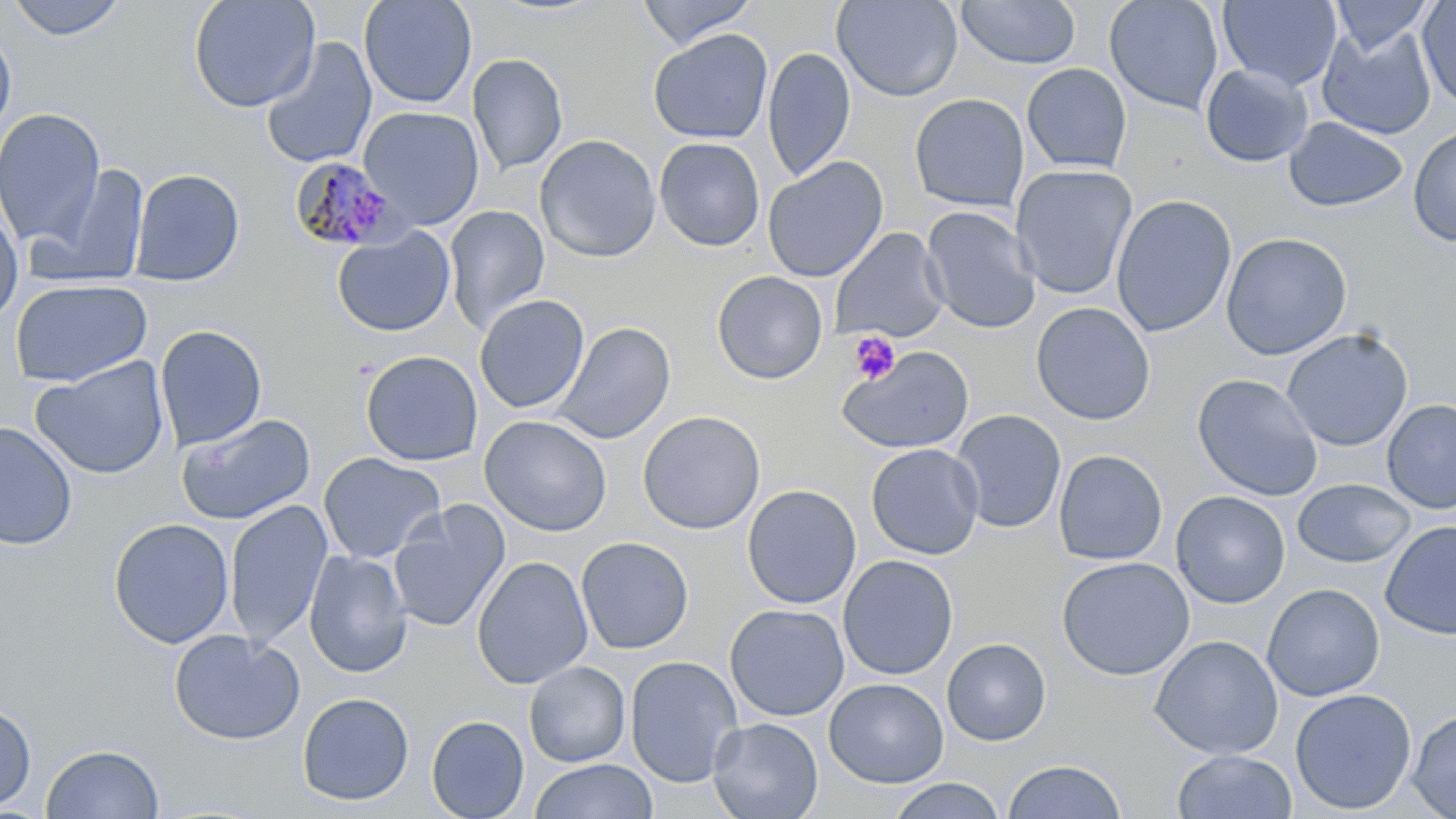
Approximate bounding boxes as (x1,y1)-(x2,y2) corner pairs in pixels. Platelet locations: (848,332)-(900,385). Plasmodium malariae-infected red blood cell locations: (288,156)-(405,254). Uninfected red blood cell locations: (6,0)-(129,42), (188,0)-(320,113), (359,0)-(477,109), (636,0)-(759,49), (832,0)-(963,102), (956,0)-(1081,69), (1104,0)-(1224,116), (1218,0)-(1342,91), (1330,0)-(1435,58), (1416,1)-(1456,109), (1317,25)-(1437,140), (0,26)-(16,140), (648,28)-(773,144), (259,37)-(378,170), (762,46)-(856,182), (467,53)-(568,175), (1021,62)-(1132,175), (1200,63)-(1314,168), (909,93)-(1029,212), (358,106)-(484,229), (0,107)-(105,248), (1283,116)-(1408,212), (1407,123)-(1456,247), (535,134)-(661,263), (654,137)-(765,251), (762,156)-(889,282), (29,164)-(151,289), (1011,164)-(1138,300), (129,168)-(245,286), (1111,194)-(1237,338), (0,203)-(24,325), (443,204)-(550,335), (920,206)-(1042,334), (332,227)-(455,337), (830,228)-(950,343), (1220,232)-(1353,360), (712,271)-(828,384), (10,278)-(153,387), (474,294)-(590,414), (1031,301)-(1156,425), (552,322)-(675,444), (155,325)-(268,450), (1281,328)-(1413,451), (837,345)-(974,454), (360,350)-(483,466), (31,357)-(170,480), (1191,373)-(1323,501), (1381,399)-(1456,514), (951,409)-(1067,534), (637,410)-(765,535), (175,413)-(316,526), (479,415)-(612,537), (191,416)-(326,632), (0,422)-(78,551), (866,443)-(984,560), (1053,449)-(1168,565), (318,452)-(445,564), (1292,478)-(1416,568), (741,484)-(861,609), (1171,491)-(1290,608), (224,500)-(333,649), (388,501)-(510,633), (108,517)-(234,649), (1380,520)-(1456,640), (575,536)-(694,654), (303,550)-(413,677), (838,554)-(958,681), (472,555)-(593,690), (1056,556)-(1195,681), (1262,583)-(1385,701), (724,603)-(850,722), (169,629)-(304,745), (1149,634)-(1284,759), (942,638)-(1051,746), (624,655)-(744,787), (524,661)-(630,767), (824,678)-(949,788), (1290,688)-(1417,814), (297,692)-(414,807), (0,702)-(37,812), (1406,709)-(1456,819), (426,715)-(529,819), (707,717)-(824,819), (41,744)-(164,819), (1172,749)-(1298,819), (529,759)-(657,819), (1002,760)-(1126,818), (887,777)-(1006,819). Slide-level diagnosis: Plasmodium malariae. Single field of view. Captured at 1000x magnification. Image is 1456×819 pixels. Light microscopy. Thin blood film. May-Grünwald-Giemsa stain.